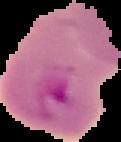
Summary:
  - Image type: cell region segmented out of the field of view; surrounding area masked to black
  - Image size: 121×142 pixels
  - Malaria status: parasitized
  - Preparation: thin blood smear